Report the malaria status of this cell.
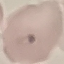
Uninfected.

{
  "stain": "Giemsa",
  "capture": "smartphone camera at the microscope eyepiece",
  "image_type": "cell patch, automatically extracted from a larger field of view and resized to 64 × 64 pixels",
  "preparation": "thin smear"
}